State the blood parasite species.
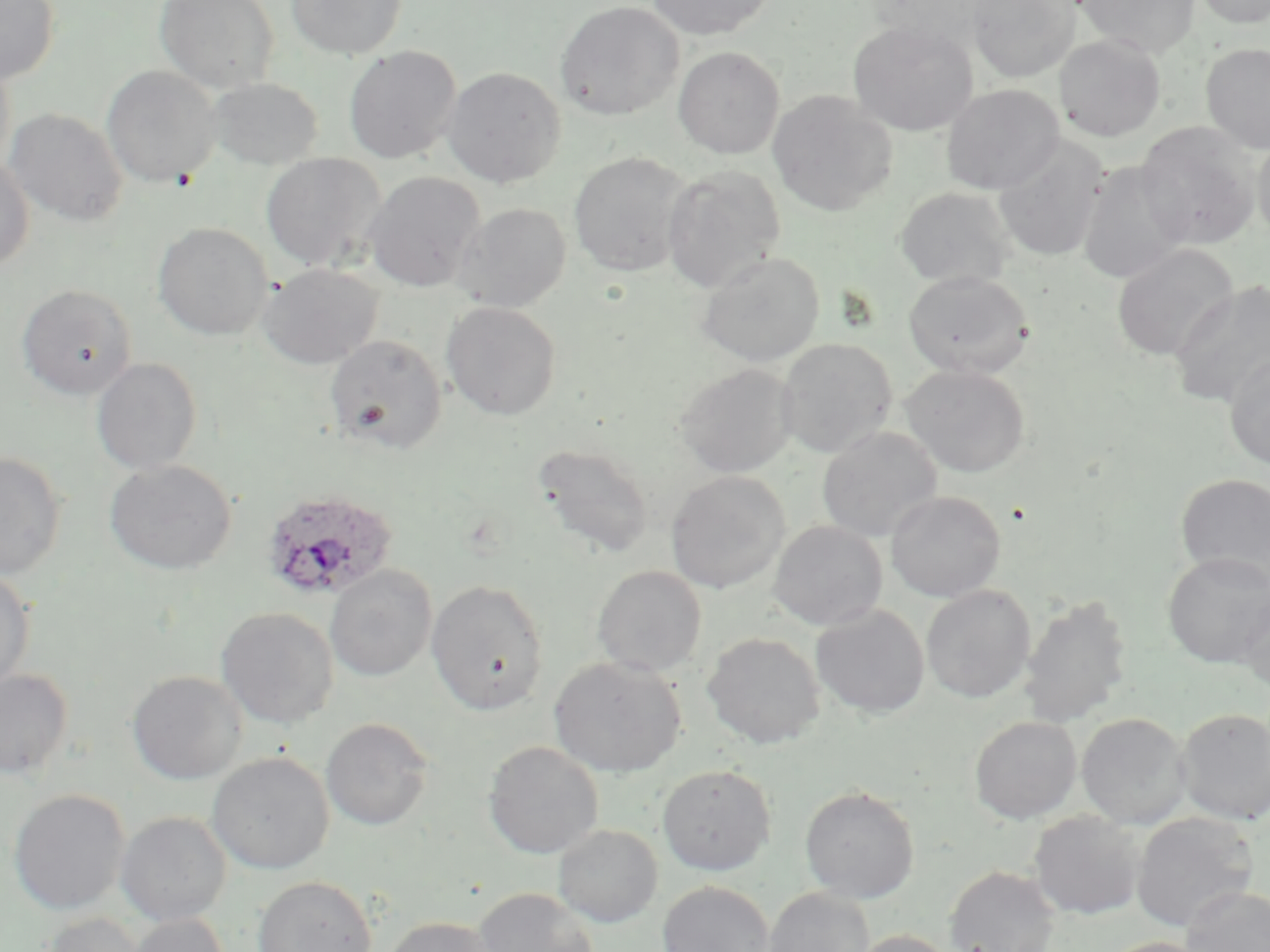
Plasmodium ovale.

Summary:
  - Coordinate format: approximate bounding boxes as (x1, y1, x2, y2) in pixels
  - Uninfected red blood cell locations: (0, 0, 59, 84), (154, 0, 280, 93), (287, 0, 407, 59), (554, 0, 685, 121), (646, 0, 775, 39), (967, 0, 1080, 83), (1076, 0, 1200, 58), (1191, 0, 1270, 28), (848, 21, 979, 136), (1054, 34, 1166, 141), (1200, 42, 1270, 154), (343, 45, 462, 164), (673, 46, 784, 158), (0, 56, 15, 177), (102, 64, 221, 187), (443, 66, 566, 187), (207, 77, 324, 170), (941, 84, 1063, 195), (767, 90, 898, 218), (5, 108, 128, 227), (1135, 122, 1262, 250), (1251, 131, 1270, 247), (992, 134, 1109, 263), (569, 151, 694, 277), (260, 153, 386, 271), (0, 155, 34, 273), (1077, 160, 1191, 284), (662, 165, 786, 293), (363, 171, 485, 292), (894, 186, 1016, 289), (452, 202, 571, 313), (152, 222, 273, 341), (1111, 244, 1239, 360), (696, 251, 825, 367), (258, 263, 383, 369), (903, 269, 1035, 379), (1169, 279, 1270, 408), (16, 284, 137, 399), (441, 301, 561, 420), (325, 334, 448, 455), (776, 337, 897, 458), (1223, 352, 1270, 470), (91, 358, 203, 475), (675, 363, 798, 478), (900, 363, 1031, 478), (817, 426, 942, 542), (532, 443, 655, 560), (0, 451, 66, 580), (104, 460, 237, 575), (666, 471, 790, 593), (1175, 473, 1270, 586), (886, 491, 1005, 602), (768, 520, 887, 631), (1163, 551, 1269, 666), (325, 564, 437, 682), (591, 565, 707, 677), (0, 568, 35, 692), (426, 579, 549, 715), (921, 585, 1036, 703), (1235, 588, 1270, 693), (1019, 595, 1131, 728), (810, 605, 930, 718), (216, 607, 339, 728), (702, 632, 825, 748), (549, 657, 686, 777), (0, 668, 73, 781), (127, 670, 247, 784), (1175, 707, 1270, 825), (1077, 713, 1191, 830), (969, 716, 1081, 824), (320, 717, 434, 831), (483, 741, 603, 859), (206, 752, 334, 874), (657, 764, 776, 875), (799, 785, 920, 903), (8, 789, 130, 914), (116, 811, 232, 925), (1029, 811, 1144, 919), (1131, 812, 1258, 932), (553, 824, 663, 928), (944, 865, 1060, 952), (252, 875, 377, 952), (657, 880, 775, 952), (1181, 886, 1270, 952), (474, 887, 599, 952), (763, 887, 874, 952), (37, 912, 146, 952), (124, 913, 229, 952), (383, 916, 502, 952), (848, 929, 958, 952), (1101, 937, 1213, 952)
  - Plasmodium ovale-infected red blood cell locations: (260, 488, 397, 602)
  - Preparation: thin blood film
  - Image size: 1270×952 pixels
  - Magnification: 1000x
  - Field of view: single
  - Stain: May-Grünwald-Giemsa
  - Modality: optical microscopy